State which parasite is depicted.
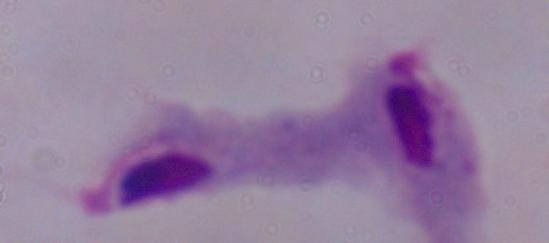
This is a trichomonad.

{
  "magnification": "1000x",
  "modality": "micrograph"
}